Locate every uninfected red blood cell.
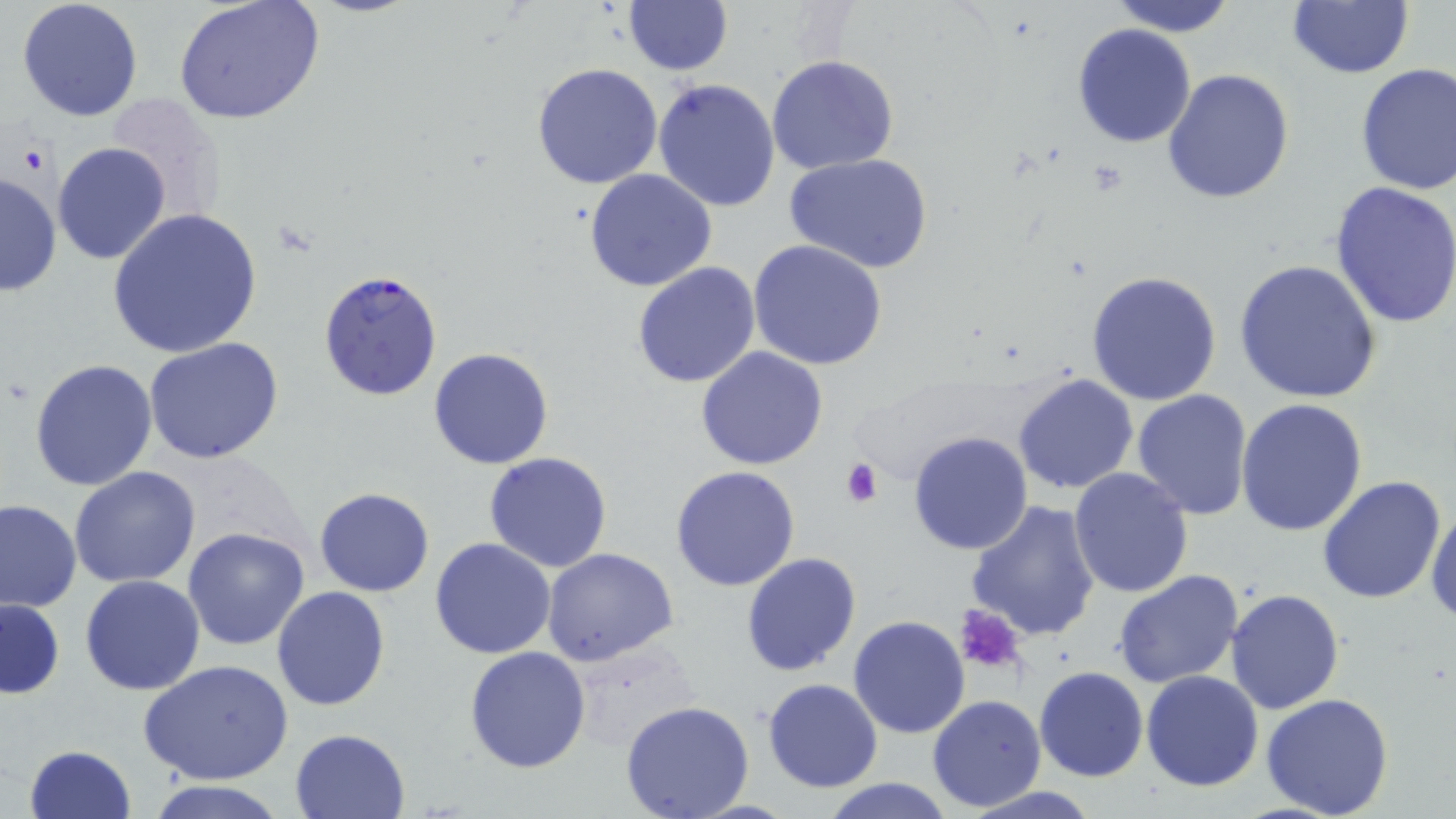
Approximate bounding boxes as [x1, y1, x2, y2] in pixels.
Uninfected red blood cells: [17, 0, 144, 121], [174, 0, 324, 126], [622, 0, 733, 75], [1108, 0, 1238, 37], [1286, 0, 1415, 79], [1071, 24, 1198, 149], [767, 55, 898, 174], [531, 62, 664, 190], [1355, 63, 1456, 198], [1162, 68, 1296, 204], [654, 78, 780, 213], [105, 93, 227, 219], [65, 109, 225, 303], [53, 142, 171, 265], [786, 155, 932, 275], [584, 169, 718, 293], [0, 172, 61, 299], [1330, 181, 1456, 328], [106, 208, 264, 358], [747, 238, 888, 371], [1236, 259, 1383, 403], [632, 261, 762, 388], [1085, 270, 1222, 407], [144, 339, 285, 465], [695, 345, 829, 469], [428, 347, 553, 469], [29, 359, 158, 491], [1013, 372, 1140, 495], [1132, 390, 1253, 521], [1237, 400, 1369, 538], [907, 430, 1034, 556], [483, 452, 614, 573], [670, 465, 802, 592], [70, 466, 203, 587], [1069, 467, 1195, 598], [1317, 475, 1447, 605], [314, 487, 436, 597], [965, 498, 1103, 642], [0, 500, 81, 613], [1427, 504, 1456, 624], [183, 526, 310, 650], [430, 536, 558, 659], [542, 546, 679, 665], [741, 552, 862, 677], [1112, 570, 1243, 690], [79, 575, 206, 695], [272, 587, 390, 711], [1225, 590, 1345, 713], [1, 598, 65, 700], [847, 615, 970, 738], [465, 646, 592, 773], [140, 659, 294, 785], [1034, 667, 1148, 782], [1140, 670, 1265, 791], [761, 678, 884, 793], [1261, 692, 1395, 819], [927, 694, 1047, 812], [620, 700, 755, 819], [290, 728, 409, 818], [22, 744, 139, 819], [817, 777, 959, 818], [143, 779, 295, 818], [952, 786, 1108, 818].

slide-level diagnosis = Plasmodium falciparum
modality = light microscopy
image size = 1456×819 pixels
Plasmodium falciparum-infected red blood cell locations = approximate bounding boxes as [x1, y1, x2, y2] in pixels: [317, 270, 445, 400]
field of view = one of a larger specimen
magnification = 1000x
platelet locations = approximate bounding boxes as [x1, y1, x2, y2] in pixels: [840, 456, 882, 506], [953, 605, 1027, 674]
preparation = thin blood smear
stain = May-Grünwald-Giemsa